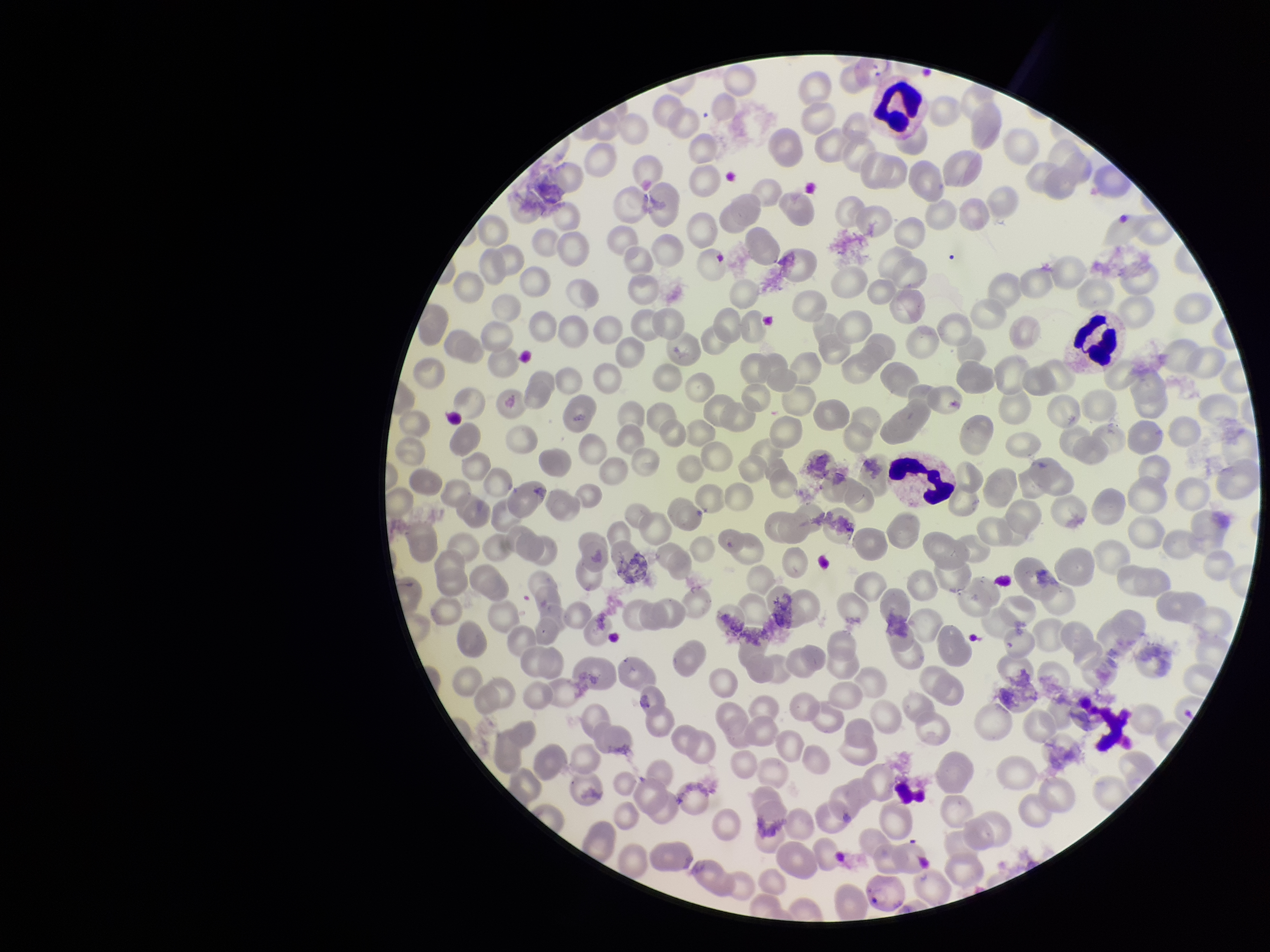
Patient malaria status: positive. Parasitized red blood cell count: 1. Photographed through the microscope eyepiece with a smartphone camera. Species reported for this patient: Plasmodium vivax. Preparation: thin. Image is 1270×952 pixels. Stained with Giemsa. Single field of view. Red blood cell count: 208. Parasitized red blood cells: seen.